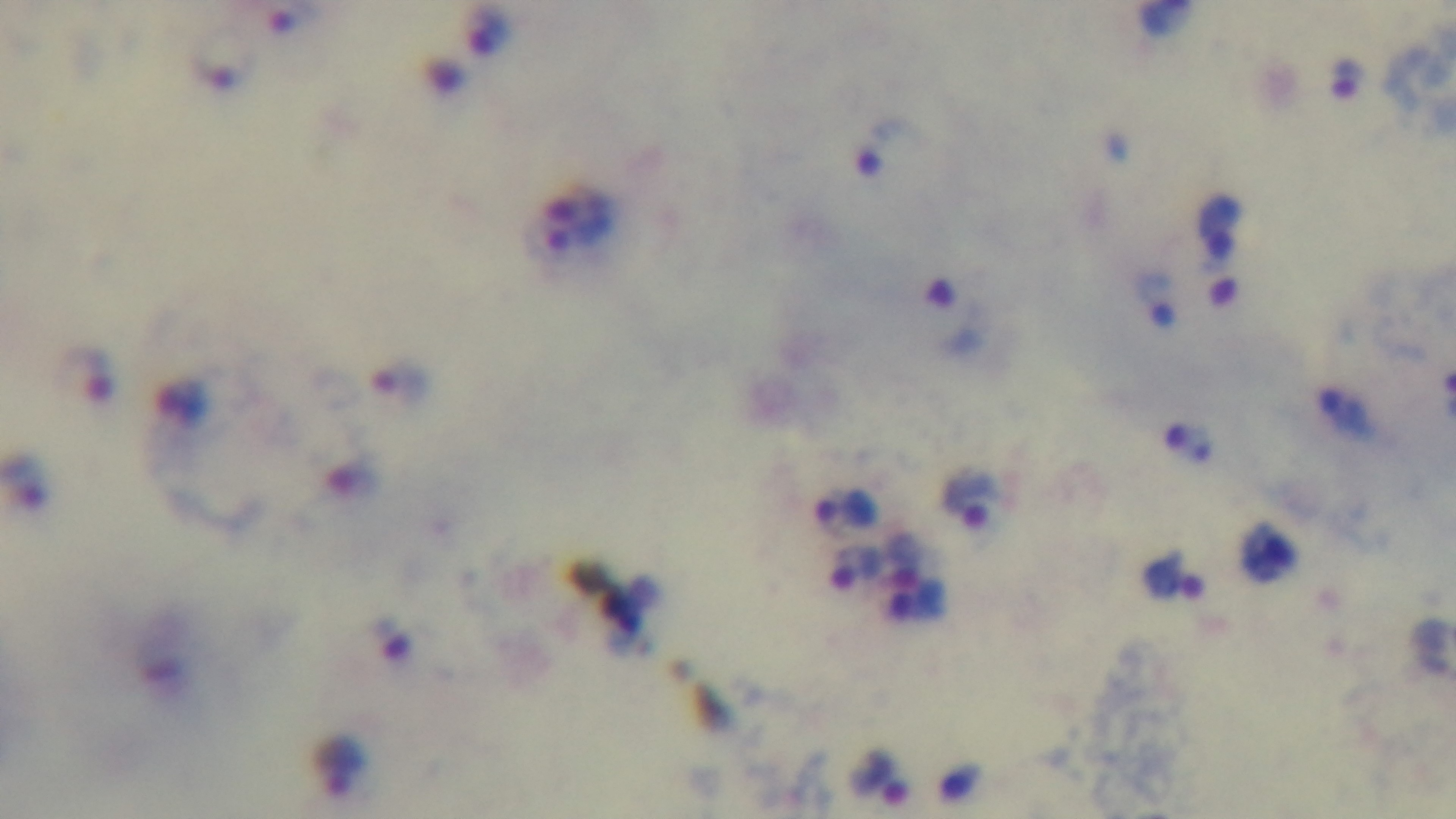
{
  "objective": "100x oil immersion",
  "field_of_view": "one from the slide",
  "stain": "Giemsa",
  "modality": "light microscopy",
  "malaria_status": "infected",
  "capture": "mounted 4K digital camera",
  "preparation": "thick blood film"
}